Comment on the morphology of the erythrocytes.
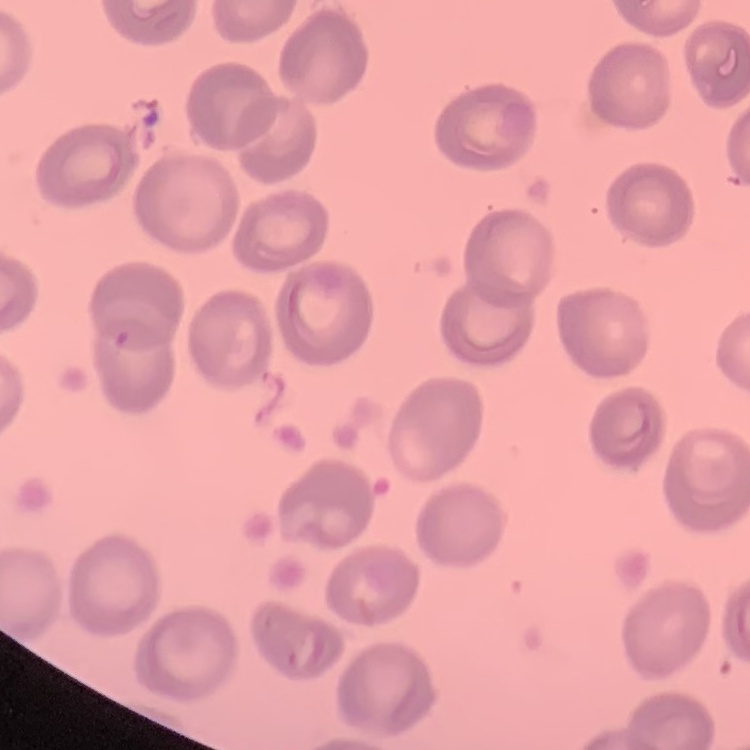

They show no rouleaux formation.

Stained with either Field's or Giemsa. One tile cut from a larger photomicrograph. Thin blood film.